Point out each leukocyte.
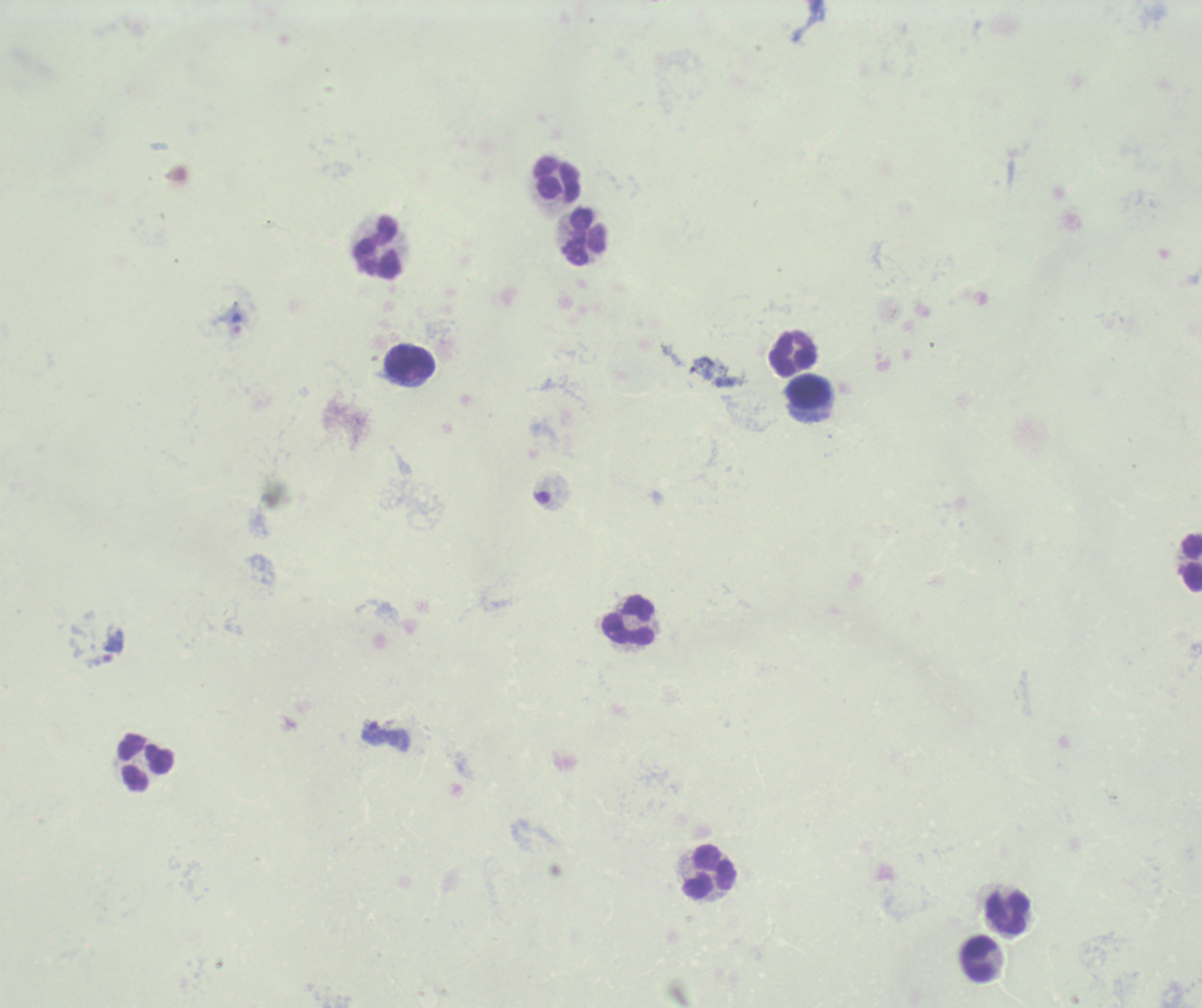

Approximate centers as {x, y} in pixels.
Leukocytes: {556, 178}, {585, 235}, {376, 246}, {795, 352}, {408, 365}, {809, 394}, {1190, 562}, {628, 620}, {144, 761}, {709, 871}, {1006, 912}, {978, 959}.

Approximate centers as {x, y} in pixels. Trophozoite locations: {236, 323}, {373, 733}. Romanowsky-stained preparation. Image is 1202×1008 pixels. Background quality: poor. Result: Plasmodium parasites detected. Previously used in a real diagnosis. Single field of view. 100x magnification. Thick blood film.